Classify this cell by malaria status.
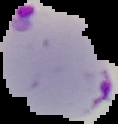

Parasitized.

The area outside the segmented cell region is set to black. Image is 118×124 pixels. From a thin blood film.